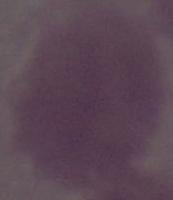
Summary:
  - Identification: red blood cell
  - Modality: micrograph
  - Magnification: 1000x